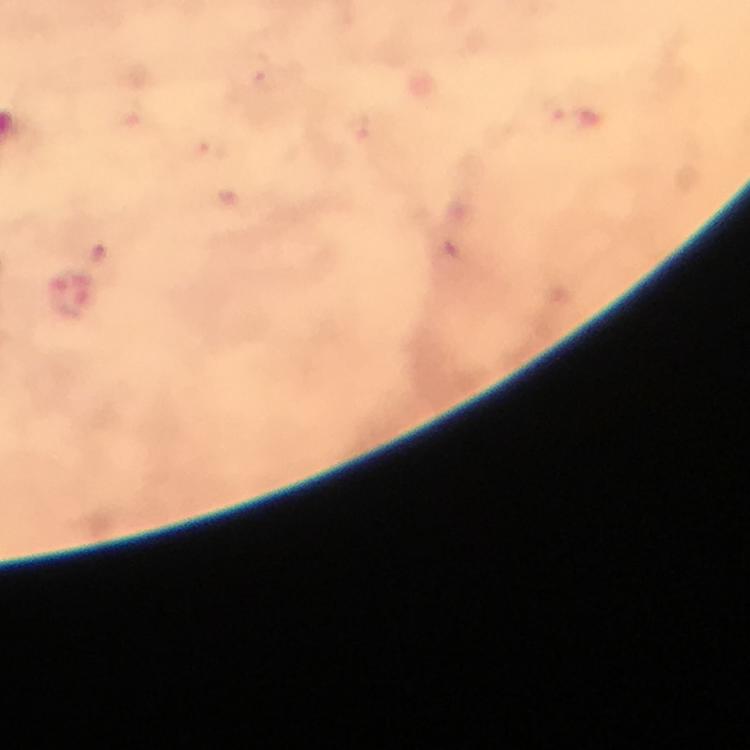 Approximate centers as {x, y} in pixels. Plasmodium parasite locations: {263, 78}, {356, 127}. From a diagnostic examination for malaria. Immersion oil was used. At 100x magnification. Image is 750×750 pixels. Photographed with a smartphone mounted on the microscope. Thick blood film. Giemsa-stained preparation. Cropped region of a single field of view.